Outline each blood parasite and name the species.
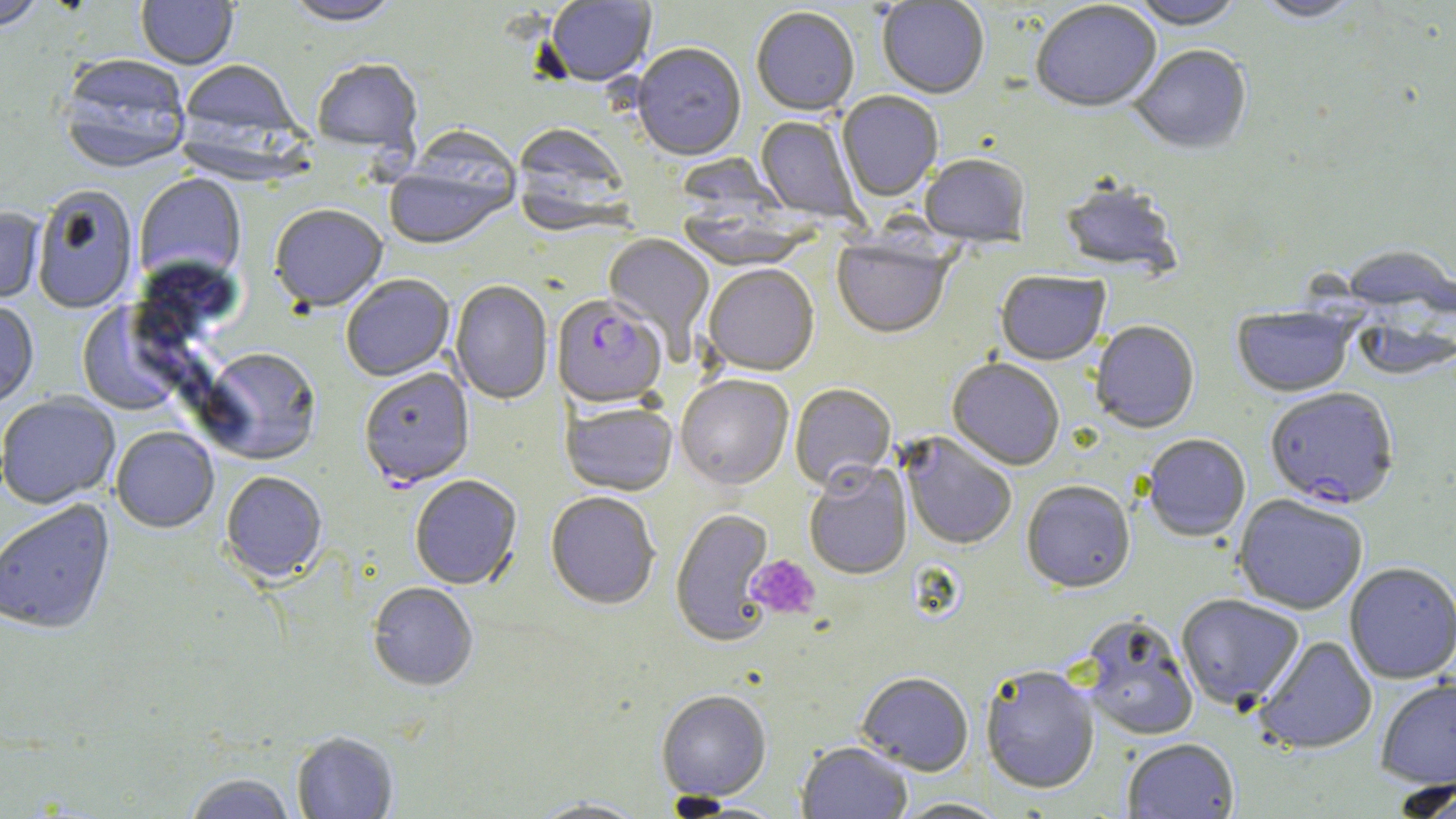
Approximate bounding boxes as named x1/y1/x2/y2 corners in pixels.
Plasmodium falciparum-infected red blood cells: (x1=552, y1=296, x2=667, y2=410), (x1=1265, y1=387, x2=1400, y2=508).
No Plasmodium ovale, Plasmodium malariae, Plasmodium vivax, Babesia divergens, or Trypanosoma brucei observed.

slide-level diagnosis = Plasmodium falciparum
preparation = thin blood smear
magnification = 1000x
field of view = single
image size = 1456×819 pixels
uninfected red blood cell locations = approximate bounding boxes as named x1/y1/x2/y2 corners in pixels: (x1=0, y1=0, x2=49, y2=32), (x1=136, y1=0, x2=238, y2=69), (x1=282, y1=0, x2=404, y2=28), (x1=877, y1=0, x2=989, y2=100), (x1=1128, y1=0, x2=1245, y2=32), (x1=1255, y1=0, x2=1364, y2=25), (x1=545, y1=1, x2=657, y2=88), (x1=1031, y1=3, x2=1161, y2=116), (x1=751, y1=8, x2=860, y2=118), (x1=632, y1=45, x2=746, y2=163), (x1=1130, y1=47, x2=1252, y2=156), (x1=58, y1=56, x2=192, y2=175), (x1=312, y1=59, x2=423, y2=156), (x1=178, y1=60, x2=302, y2=147), (x1=837, y1=92, x2=943, y2=203), (x1=755, y1=116, x2=862, y2=224), (x1=512, y1=124, x2=632, y2=235), (x1=385, y1=148, x2=518, y2=252), (x1=674, y1=153, x2=789, y2=221), (x1=919, y1=156, x2=1030, y2=249), (x1=134, y1=174, x2=246, y2=287), (x1=1058, y1=182, x2=1182, y2=277), (x1=32, y1=186, x2=138, y2=314), (x1=269, y1=206, x2=388, y2=315), (x1=0, y1=208, x2=45, y2=306), (x1=677, y1=208, x2=816, y2=272), (x1=603, y1=234, x2=715, y2=355), (x1=832, y1=236, x2=954, y2=341), (x1=703, y1=266, x2=819, y2=378), (x1=689, y1=268, x2=808, y2=491), (x1=996, y1=272, x2=1110, y2=366), (x1=341, y1=275, x2=454, y2=382), (x1=450, y1=280, x2=553, y2=406), (x1=76, y1=299, x2=191, y2=417), (x1=0, y1=301, x2=39, y2=410), (x1=1232, y1=306, x2=1356, y2=397), (x1=1350, y1=311, x2=1455, y2=381), (x1=1090, y1=322, x2=1199, y2=434), (x1=200, y1=349, x2=321, y2=466), (x1=947, y1=359, x2=1065, y2=471), (x1=359, y1=369, x2=475, y2=490), (x1=676, y1=376, x2=793, y2=490), (x1=790, y1=384, x2=896, y2=493), (x1=0, y1=394, x2=120, y2=509), (x1=561, y1=402, x2=678, y2=496), (x1=111, y1=427, x2=219, y2=533), (x1=901, y1=434, x2=1017, y2=550), (x1=1142, y1=434, x2=1250, y2=542), (x1=804, y1=463, x2=913, y2=580), (x1=220, y1=472, x2=327, y2=586), (x1=410, y1=475, x2=522, y2=591), (x1=1021, y1=481, x2=1135, y2=594), (x1=546, y1=492, x2=660, y2=611), (x1=1233, y1=494, x2=1368, y2=614), (x1=1, y1=499, x2=116, y2=637), (x1=670, y1=509, x2=775, y2=647), (x1=1343, y1=561, x2=1456, y2=683), (x1=368, y1=583, x2=478, y2=692), (x1=1176, y1=593, x2=1305, y2=710), (x1=1076, y1=614, x2=1200, y2=741), (x1=1254, y1=635, x2=1378, y2=754), (x1=981, y1=665, x2=1100, y2=794), (x1=856, y1=672, x2=974, y2=776), (x1=1375, y1=676, x2=1456, y2=788), (x1=656, y1=691, x2=772, y2=802), (x1=292, y1=733, x2=398, y2=818), (x1=1122, y1=737, x2=1239, y2=818), (x1=796, y1=742, x2=912, y2=818), (x1=183, y1=772, x2=297, y2=818), (x1=1387, y1=779, x2=1456, y2=818), (x1=527, y1=797, x2=651, y2=818), (x1=892, y1=797, x2=1010, y2=818)
platelet locations = approximate bounding boxes as named x1/y1/x2/y2 corners in pixels: (x1=747, y1=554, x2=821, y2=620)
modality = optical microscopy
stain = May-Grünwald-Giemsa